Name the parasite shown.
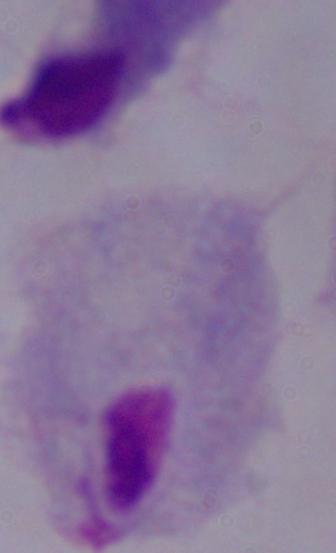
A trichomonad.

Photomicrograph. Captured at 1000x magnification.